Classify the preparation.
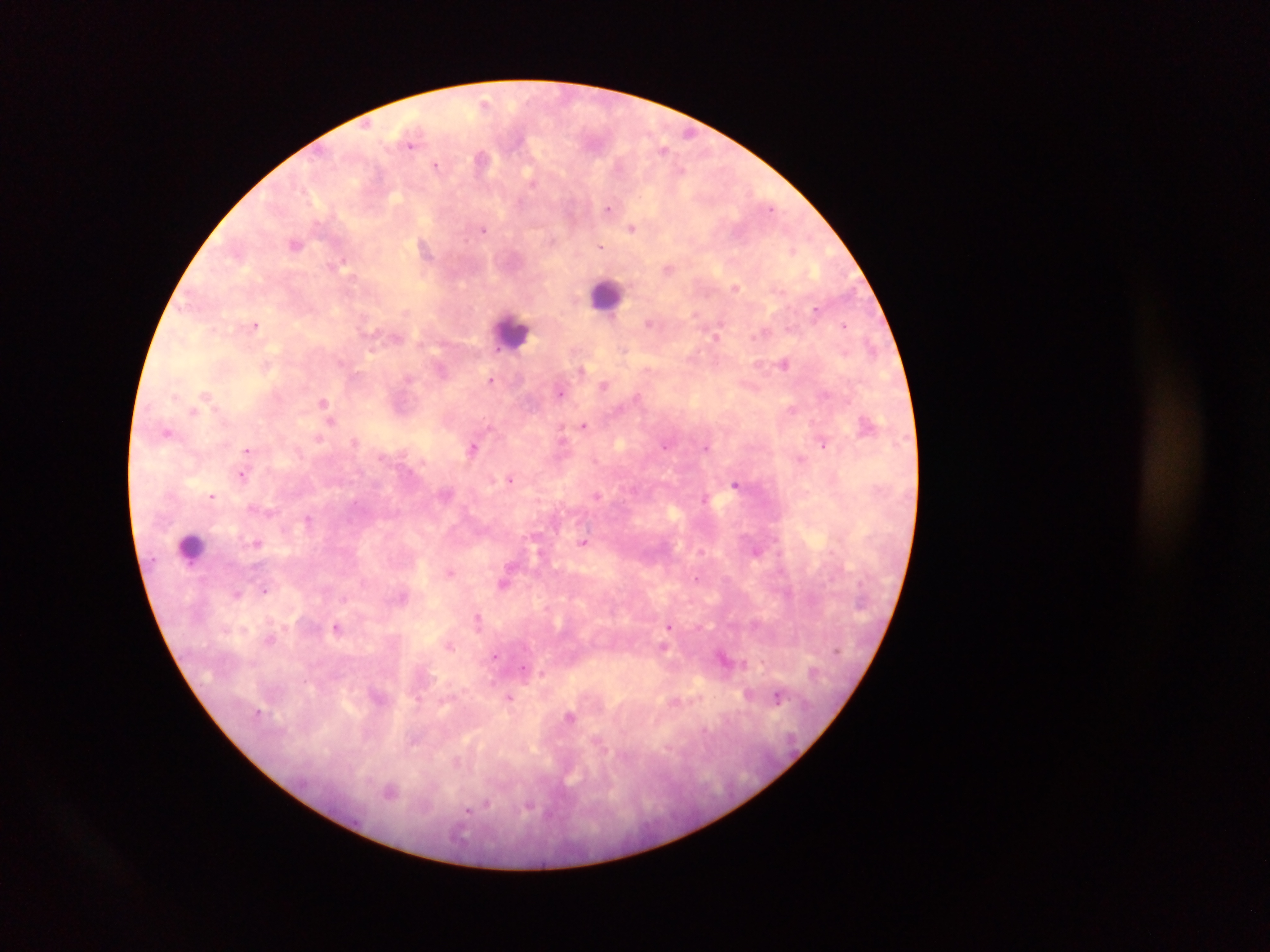

This is a thick smear.

Approximate centers as {x, y} in pixels. Plasmodium parasite locations: {485, 104}, {410, 141}, {663, 149}, {483, 157}, {436, 166}, {610, 207}, {632, 228}, {483, 229}, {296, 243}, {600, 246}, {344, 263}, {669, 268}, {736, 287}, {816, 309}, {649, 322}, {256, 324}, {845, 325}, {717, 335}, {784, 363}, {582, 369}, {491, 379}, {604, 385}, {561, 392}, {207, 394}, {324, 402}, {194, 410}, {331, 419}, {867, 424}, {585, 425}, {168, 431}, {319, 438}, {355, 442}, {822, 443}, {665, 446}, {473, 447}, {707, 447}, {248, 450}, {243, 474}, {511, 478}, {736, 484}, {212, 495}, {596, 495}, {705, 499}, {252, 507}, {309, 519}, {258, 542}, {585, 543}, {757, 550}, {451, 572}, {505, 582}, {265, 589}, {238, 592}, {479, 619}, {671, 625}, {338, 628}, {450, 645}, {663, 648}, {497, 656}, {725, 659}, {541, 672}, {750, 694}, {779, 697}, {510, 698}, {571, 716}, {390, 791}. Leukocyte locations: {607, 294}, {511, 330}, {192, 546}. Image is 1270×952 pixels. One field of view. Photographed through a microscope with a mobile-phone camera. Sample from Ghana.